Describe the morphology of the erythrocytes.
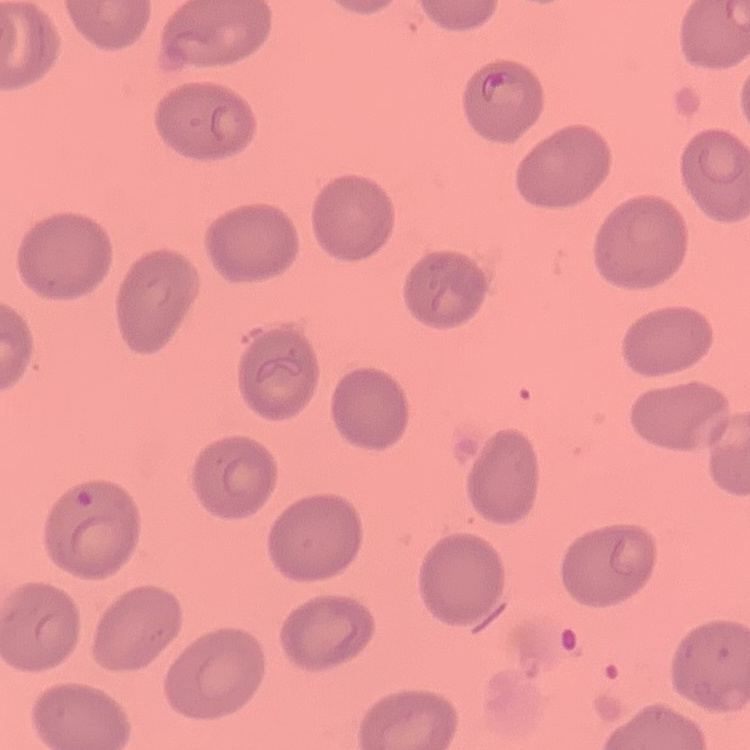

They show no rouleaux formation.

Square crop of a larger photomicrograph. Stained with either Field's or Giemsa. Thin peripheral smear.